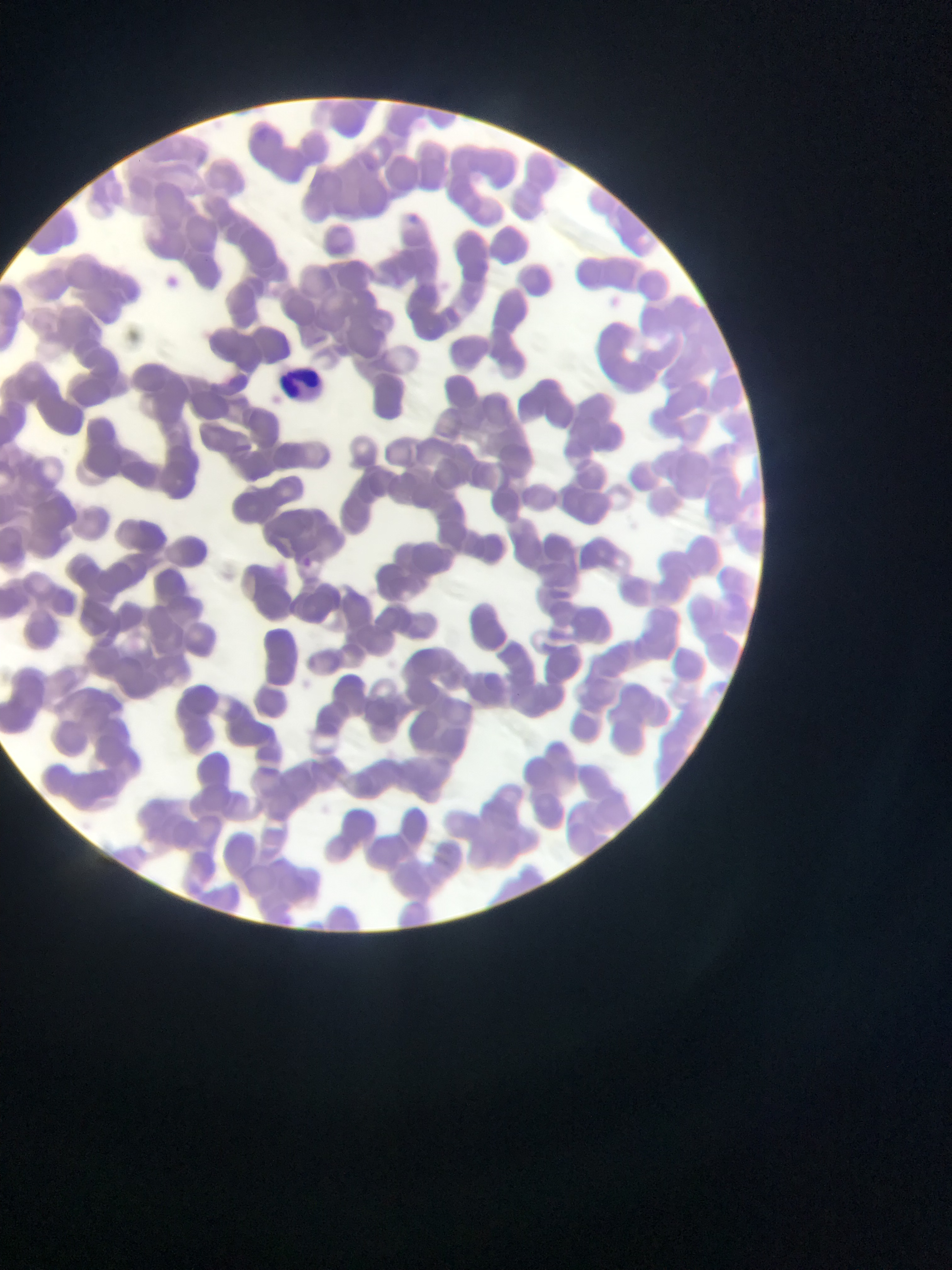

Approximate bounding boxes as left top right bottom in pixels. Leukocyte locations: 279 364 329 410. Malaria parasite locations: 297 557 322 574. Thin blood film. One field of view. Image is 952×1270 pixels. Collected in Ghana. Mobile-phone photograph taken through the microscope.